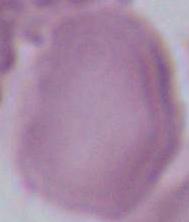

Summary:
  - Identification: red blood cell
  - Magnification: 1000x
  - Modality: photomicrograph